Report the malaria status of this cell.
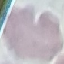
Uninfected.

Summary:
  - Stain: Giemsa
  - Image type: automatically extracted cell patch, resized to 64 × 64 pixels
  - Capture: smartphone through the microscope eyepiece
  - Preparation: thin blood smear